Comment on the morphology of the erythrocytes.
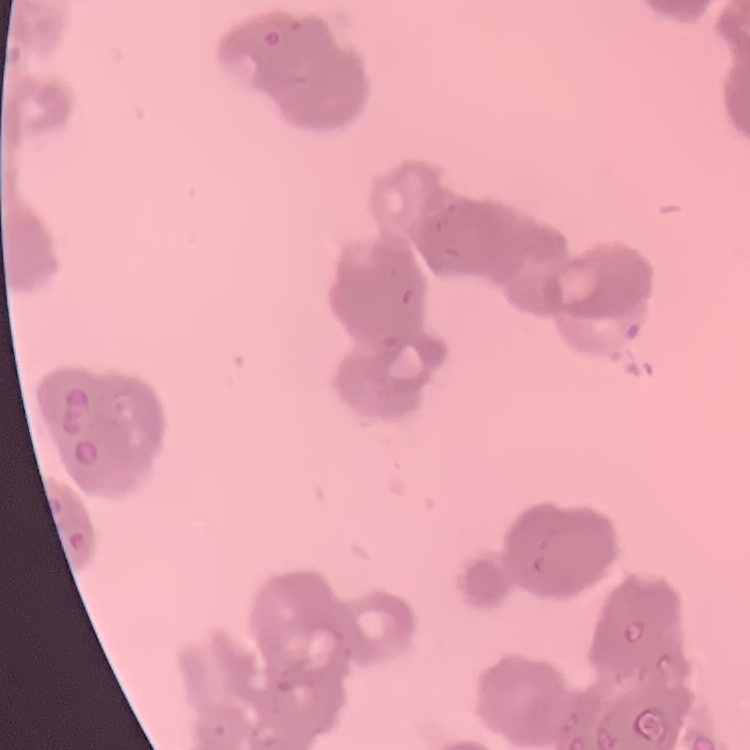

They show rouleaux formation.

Summary:
  - Image type: one tile cut from a larger photomicrograph
  - Preparation: thin peripheral smear
  - Stain: Field's or Giemsa